Report the malaria status of this cell.
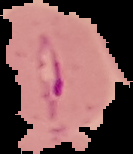
It is parasitized.

{
  "image_size": "133×154 pixels",
  "preparation": "thin blood film",
  "image_type": "cell region segmented out of the field of view; surrounding area masked to black"
}